Assess this cell for malaria.
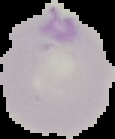
Parasitized.

{
  "image_size": "115×139 pixels",
  "image_type": "cell region segmented out of the field of view; surrounding area masked to black",
  "preparation": "thin blood smear"
}